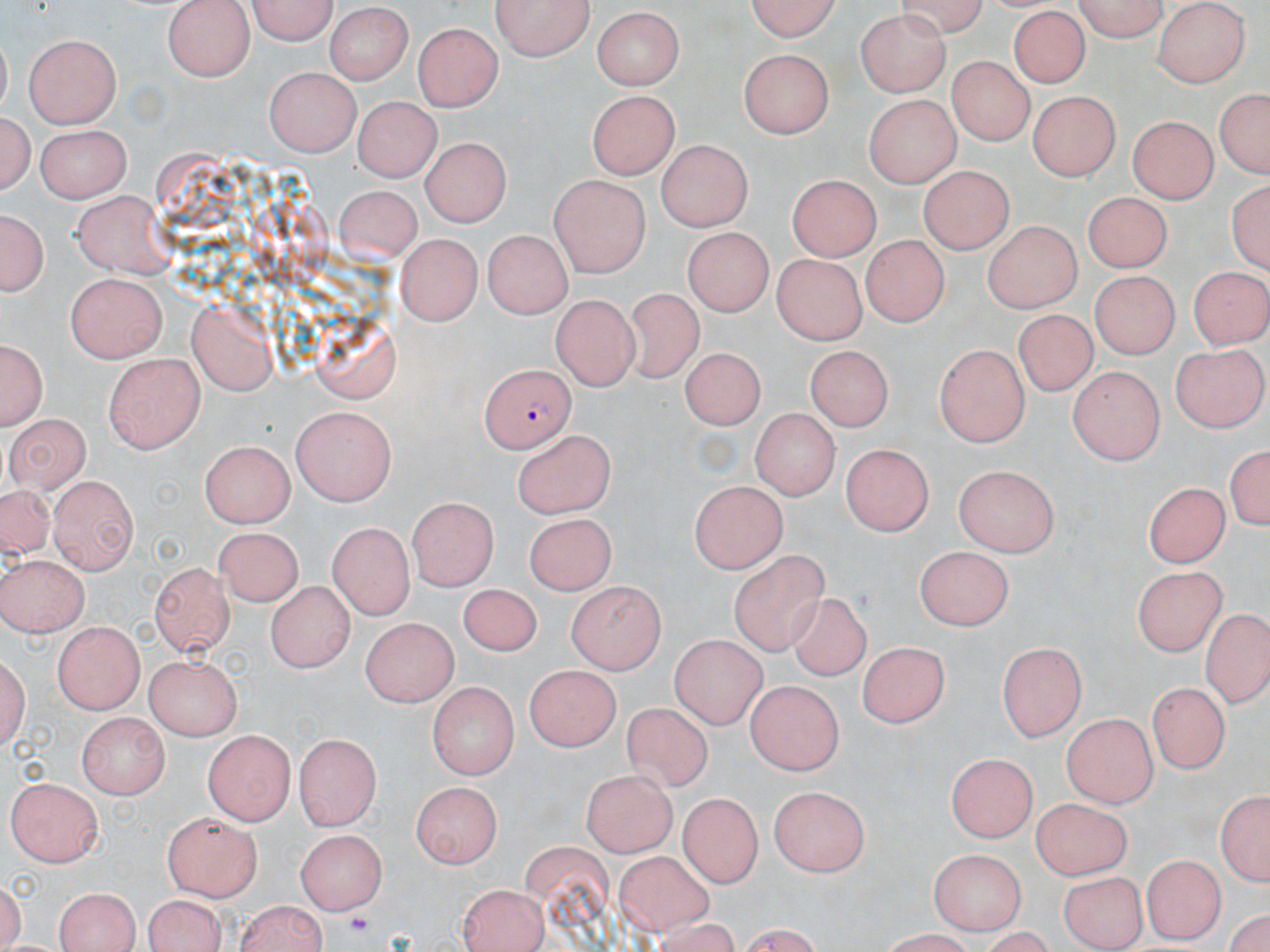
Approximate bounding boxes as (x1,y1)-(x2,y2) corner pairs in pixels. Uninfected red blood cell locations: (241,0)-(338,44), (495,0)-(595,60), (742,0)-(849,42), (1067,0)-(1170,40), (164,1)-(255,81), (1154,3)-(1251,89), (326,5)-(413,84), (590,8)-(687,89), (1006,9)-(1094,89), (858,12)-(951,97), (414,25)-(501,112), (23,33)-(122,130), (740,48)-(837,136), (947,56)-(1032,145), (262,65)-(363,155), (1212,86)-(1269,180), (585,88)-(679,179), (1028,90)-(1120,182), (863,94)-(961,185), (354,97)-(438,180), (2,105)-(36,200), (1129,114)-(1218,201), (33,123)-(132,199), (417,130)-(510,222), (655,139)-(752,231), (919,165)-(1013,255), (548,169)-(648,273), (789,173)-(878,262), (1228,181)-(1267,273), (331,187)-(424,268), (72,190)-(180,278), (1085,193)-(1171,271), (1,204)-(51,298), (984,221)-(1081,314), (682,226)-(777,314), (395,232)-(481,327), (482,232)-(573,317), (861,234)-(948,326), (770,255)-(867,343), (1186,262)-(1267,353), (1092,268)-(1183,359), (66,272)-(169,361), (618,291)-(707,384), (553,292)-(639,384), (183,300)-(279,394), (1008,313)-(1094,398), (2,335)-(46,428), (679,336)-(758,432), (933,341)-(1029,447), (1172,343)-(1269,431), (804,348)-(894,437), (103,352)-(205,452), (1066,367)-(1165,463), (290,406)-(394,507), (748,408)-(839,501), (4,414)-(88,492), (514,429)-(619,519), (199,439)-(293,526), (1221,439)-(1268,539), (839,440)-(933,535), (951,464)-(1062,554), (47,474)-(139,573), (1141,479)-(1232,566), (687,480)-(789,572), (0,486)-(59,570), (403,501)-(495,591), (521,510)-(615,596), (326,521)-(416,617), (216,524)-(308,605), (912,546)-(1017,628), (729,549)-(834,657), (0,557)-(87,634), (149,563)-(237,654), (1132,568)-(1223,657), (264,578)-(353,673), (566,580)-(665,674), (456,582)-(544,657), (784,589)-(873,682), (1202,610)-(1270,711), (362,613)-(463,705), (52,620)-(143,714), (668,634)-(768,727), (994,638)-(1087,740), (857,643)-(953,730), (2,648)-(31,758), (144,652)-(244,739), (522,662)-(619,750), (427,677)-(514,778), (743,678)-(843,776), (1152,680)-(1231,768), (623,703)-(711,791), (76,711)-(168,799), (1061,712)-(1160,806), (204,730)-(296,823), (295,733)-(382,827), (947,752)-(1038,843), (580,763)-(679,855), (7,776)-(104,867), (412,780)-(504,867), (768,785)-(868,875), (1213,786)-(1270,890), (679,791)-(764,889), (1029,802)-(1133,877), (162,810)-(262,899), (297,826)-(387,914), (519,844)-(615,932), (928,846)-(1026,932), (613,849)-(717,935), (1141,852)-(1223,943), (1058,869)-(1146,948), (456,881)-(551,952), (51,886)-(147,951), (140,895)-(227,952), (231,899)-(328,952). Plasmodium falciparum-infected red blood cell locations: (478,364)-(573,450). Slide-level diagnosis: Plasmodium falciparum. Image is 1270×952 pixels. Thin blood smear. One field of a larger specimen. 1000x magnification. Optical microscopy. May-Grünwald-Giemsa stain.